Report the malaria status of this cell.
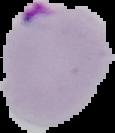
Parasitized.

image_type: segmented cell region with the area outside set to black
preparation: thin blood smear
image_size: 115×133 pixels